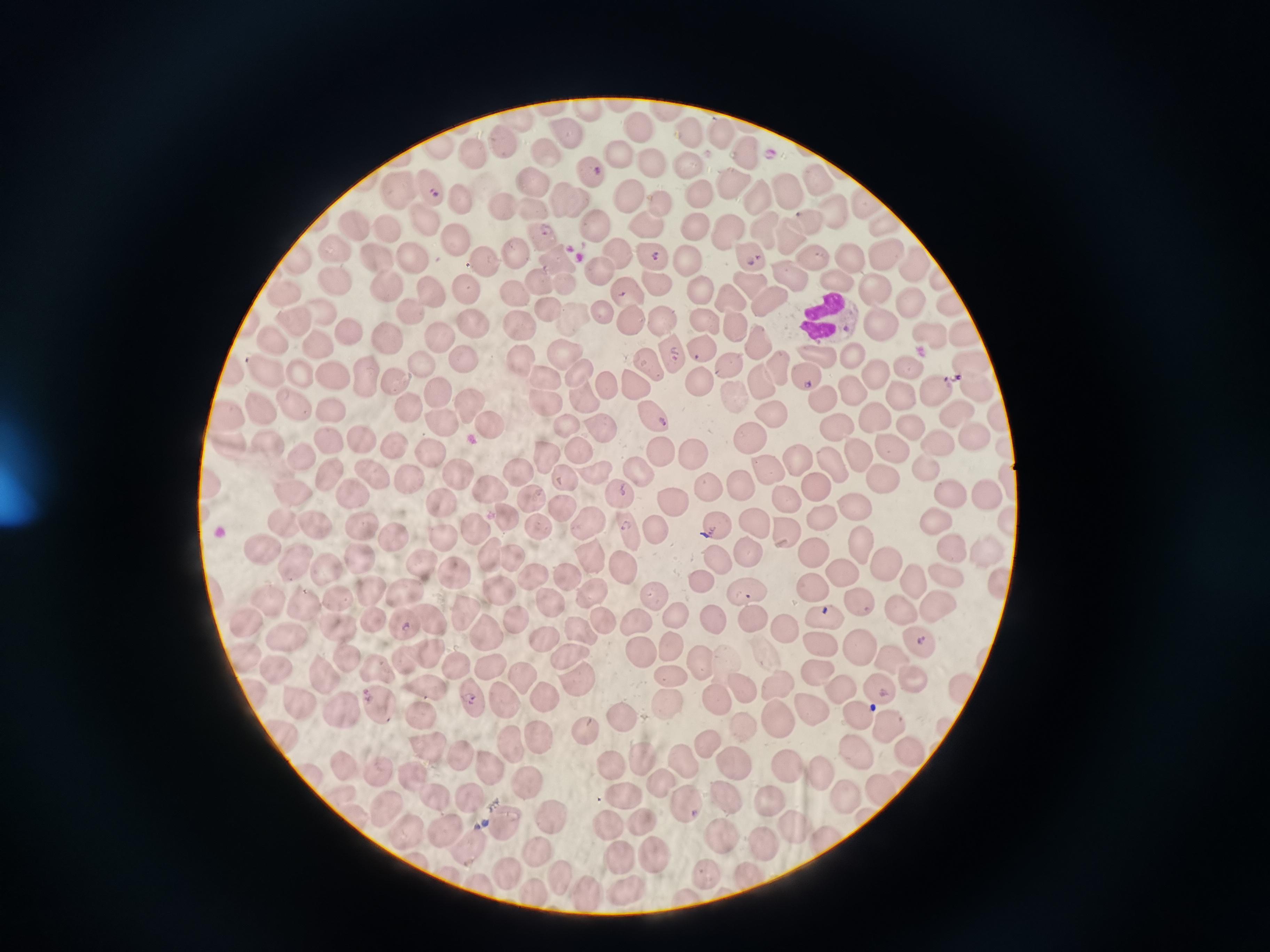

Approximate object centers, in pixels from the top-left corner. Cell locations: (x=588, y=108), (x=637, y=126), (x=566, y=131), (x=718, y=134), (x=688, y=135), (x=501, y=143), (x=437, y=148), (x=744, y=152), (x=619, y=153), (x=546, y=154), (x=473, y=155), (x=654, y=164), (x=690, y=164), (x=590, y=174), (x=815, y=177), (x=735, y=179), (x=529, y=183), (x=428, y=186), (x=399, y=191), (x=783, y=191), (x=699, y=192), (x=755, y=193), (x=567, y=198), (x=629, y=198), (x=462, y=200), (x=657, y=202), (x=867, y=202), (x=502, y=208), (x=529, y=209), (x=832, y=209), (x=424, y=221), (x=806, y=221), (x=886, y=223), (x=646, y=224), (x=592, y=225), (x=694, y=225), (x=352, y=226), (x=386, y=229), (x=727, y=230), (x=766, y=230), (x=789, y=234), (x=541, y=236), (x=456, y=239), (x=332, y=248), (x=515, y=252), (x=617, y=254), (x=745, y=254), (x=882, y=254), (x=553, y=256), (x=652, y=256), (x=377, y=257), (x=413, y=258), (x=844, y=258), (x=295, y=259), (x=690, y=261), (x=810, y=261), (x=482, y=262), (x=913, y=265), (x=598, y=268), (x=794, y=277), (x=939, y=279), (x=539, y=281), (x=657, y=282), (x=840, y=282), (x=334, y=283), (x=565, y=284), (x=387, y=285), (x=746, y=285), (x=702, y=286), (x=466, y=288), (x=876, y=288), (x=429, y=290), (x=283, y=293), (x=628, y=296), (x=511, y=298), (x=732, y=301), (x=907, y=301), (x=768, y=302), (x=952, y=308), (x=409, y=310), (x=548, y=310), (x=599, y=312), (x=320, y=314), (x=574, y=315), (x=628, y=318), (x=661, y=319), (x=702, y=321), (x=880, y=321), (x=297, y=322), (x=518, y=323), (x=469, y=324), (x=737, y=326), (x=348, y=330), (x=388, y=335), (x=436, y=336), (x=930, y=336), (x=963, y=337), (x=754, y=342), (x=275, y=343), (x=318, y=345), (x=701, y=345), (x=562, y=350), (x=674, y=354), (x=520, y=356), (x=818, y=356), (x=850, y=356), (x=461, y=359), (x=967, y=361), (x=418, y=363), (x=649, y=364), (x=730, y=368), (x=779, y=368), (x=909, y=368), (x=298, y=372), (x=577, y=372), (x=265, y=374), (x=363, y=374), (x=874, y=374), (x=330, y=375), (x=543, y=376), (x=805, y=376), (x=396, y=381), (x=759, y=381), (x=603, y=383), (x=698, y=383), (x=633, y=385), (x=975, y=388), (x=935, y=389), (x=851, y=390), (x=438, y=393), (x=734, y=393), (x=583, y=394), (x=899, y=394), (x=295, y=398), (x=546, y=400), (x=466, y=401), (x=330, y=408), (x=261, y=409), (x=407, y=409), (x=957, y=412), (x=225, y=413), (x=771, y=414), (x=873, y=417), (x=649, y=418), (x=436, y=420), (x=485, y=421), (x=563, y=423), (x=910, y=425), (x=1000, y=425), (x=600, y=427), (x=839, y=428), (x=971, y=435), (x=749, y=436), (x=365, y=439), (x=329, y=440), (x=936, y=441), (x=394, y=442), (x=890, y=442), (x=265, y=444), (x=1006, y=448), (x=576, y=449), (x=431, y=452), (x=854, y=454), (x=660, y=457), (x=692, y=458), (x=299, y=459), (x=546, y=460), (x=796, y=460), (x=830, y=464), (x=925, y=468), (x=454, y=470), (x=765, y=470), (x=324, y=471), (x=518, y=472), (x=372, y=473), (x=639, y=474), (x=589, y=477), (x=407, y=479), (x=885, y=479), (x=564, y=482), (x=211, y=483), (x=706, y=483), (x=737, y=483), (x=815, y=484), (x=489, y=486), (x=353, y=490), (x=294, y=491), (x=618, y=493), (x=985, y=493), (x=948, y=494), (x=669, y=496), (x=531, y=498), (x=784, y=501), (x=851, y=504), (x=441, y=505), (x=560, y=508), (x=505, y=513), (x=821, y=514), (x=935, y=520), (x=1008, y=520), (x=283, y=522), (x=538, y=522), (x=588, y=524), (x=716, y=524), (x=753, y=524), (x=362, y=527), (x=310, y=528), (x=474, y=529), (x=628, y=529), (x=784, y=530), (x=653, y=535), (x=442, y=536), (x=390, y=538), (x=859, y=543), (x=948, y=546), (x=261, y=549), (x=984, y=550), (x=746, y=552), (x=489, y=554), (x=812, y=554), (x=589, y=557), (x=511, y=558), (x=422, y=559), (x=718, y=561), (x=294, y=563), (x=358, y=563), (x=620, y=563), (x=886, y=565), (x=326, y=570), (x=447, y=570), (x=844, y=571), (x=563, y=573), (x=941, y=574), (x=912, y=578), (x=535, y=579), (x=698, y=583), (x=1000, y=583), (x=497, y=585), (x=811, y=585), (x=744, y=590), (x=591, y=592), (x=368, y=595), (x=651, y=595), (x=409, y=596), (x=339, y=599), (x=857, y=600), (x=264, y=603), (x=552, y=606), (x=939, y=606), (x=302, y=608), (x=896, y=612), (x=680, y=616), (x=822, y=617), (x=514, y=619), (x=599, y=619), (x=712, y=619), (x=372, y=620), (x=754, y=620), (x=430, y=621), (x=465, y=621), (x=637, y=622), (x=243, y=623), (x=405, y=626), (x=340, y=630), (x=783, y=631), (x=284, y=633), (x=583, y=635), (x=486, y=636), (x=543, y=637), (x=919, y=642), (x=822, y=645), (x=673, y=647), (x=856, y=649), (x=639, y=650), (x=569, y=653), (x=240, y=654), (x=427, y=655), (x=345, y=658), (x=699, y=661), (x=409, y=662), (x=890, y=662), (x=376, y=664), (x=488, y=666), (x=278, y=668), (x=456, y=668), (x=818, y=672), (x=667, y=674), (x=325, y=676), (x=517, y=676), (x=907, y=676), (x=577, y=685), (x=742, y=687), (x=777, y=687), (x=425, y=690), (x=959, y=690), (x=875, y=691), (x=841, y=694), (x=541, y=696), (x=476, y=699), (x=713, y=700), (x=299, y=704), (x=503, y=704), (x=339, y=708), (x=664, y=708), (x=807, y=708), (x=380, y=711), (x=857, y=715), (x=420, y=717), (x=775, y=719), (x=617, y=720), (x=886, y=725), (x=738, y=726), (x=579, y=732), (x=284, y=733), (x=538, y=740), (x=705, y=744), (x=428, y=747), (x=509, y=747), (x=855, y=749), (x=906, y=749), (x=463, y=756), (x=640, y=759), (x=682, y=760), (x=603, y=762), (x=732, y=762), (x=344, y=763), (x=786, y=764), (x=487, y=766), (x=383, y=770), (x=819, y=771), (x=310, y=772), (x=416, y=774), (x=659, y=780), (x=527, y=785), (x=622, y=791), (x=841, y=791), (x=878, y=791), (x=470, y=796), (x=435, y=798), (x=770, y=798), (x=725, y=800), (x=689, y=806), (x=387, y=807), (x=637, y=816), (x=550, y=817), (x=505, y=822), (x=788, y=822), (x=442, y=826), (x=607, y=826), (x=407, y=827), (x=718, y=836), (x=828, y=838), (x=469, y=841), (x=762, y=843), (x=540, y=851), (x=652, y=851), (x=616, y=855), (x=505, y=870), (x=701, y=870), (x=561, y=881), (x=629, y=885), (x=531, y=890), (x=586, y=891). Malaria reading: positive. Image is 1270×952 pixels. Giemsa stain. Thin blood film. One field from this slide. Photographed with a smartphone camera at the microscope eyepiece.